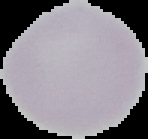

preparation = thin blood film
result = no malaria parasites detected
image size = 148×139 pixels
image type = segmented cell region with the area outside set to black